Assess the morphology of the red blood cells.
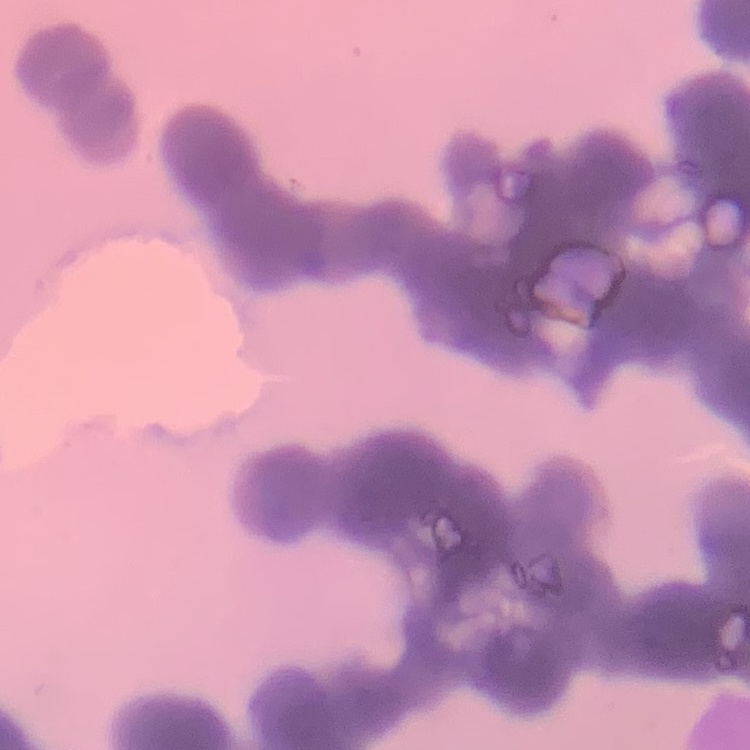

They show rouleaux formation.

Thin blood film. One tile cut from a larger photomicrograph. Stained with either Field's or Giemsa.